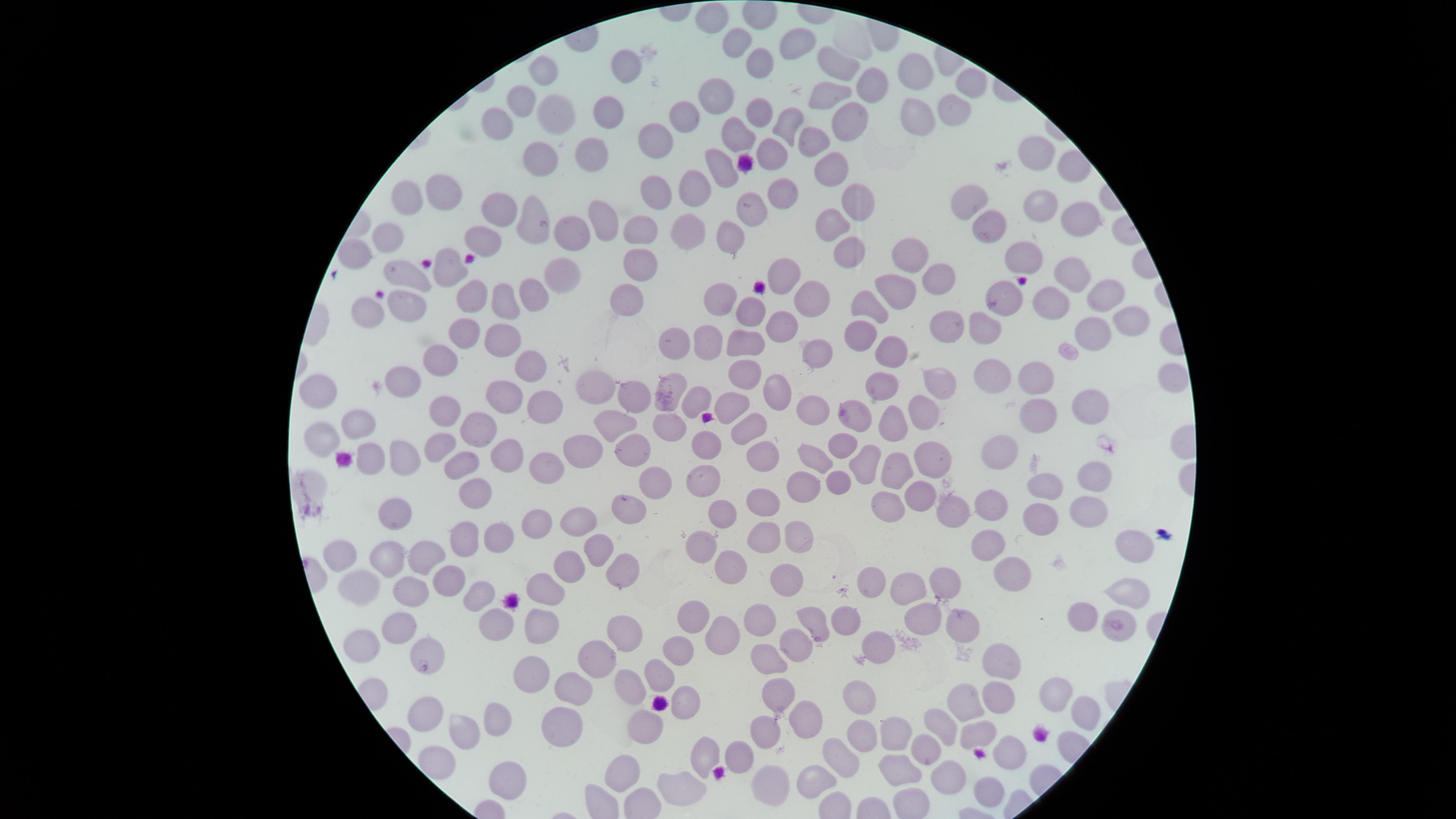
Approximate marker points as [x, y] in pixels. Uninfected RBCs: [712, 15], [790, 44], [732, 46], [762, 64], [625, 66], [838, 68], [917, 68], [547, 75], [873, 80], [969, 80], [718, 93], [835, 99], [525, 102], [950, 111], [561, 112], [612, 112], [760, 113], [680, 116], [916, 119], [850, 122], [502, 123], [781, 125], [736, 137], [818, 139], [654, 140], [540, 151], [1036, 151], [775, 153], [588, 159], [829, 170], [724, 175], [696, 189], [782, 193], [444, 194], [407, 198], [854, 201], [971, 201], [657, 202], [1039, 206], [500, 208], [755, 208], [532, 220], [604, 220], [1074, 220], [691, 229], [985, 231], [832, 232], [737, 234], [569, 236], [389, 237], [485, 239], [636, 239], [848, 249], [916, 253], [1024, 254], [360, 255], [447, 267], [644, 267], [1069, 271], [407, 273], [788, 273], [937, 274], [560, 279], [899, 285], [1006, 288], [1095, 290], [465, 297], [530, 298], [630, 298], [721, 298], [809, 299], [1050, 299], [496, 304], [871, 304], [405, 306], [750, 313], [371, 314], [783, 323], [1130, 323], [955, 324], [988, 325], [865, 329], [459, 334], [496, 338], [711, 338], [748, 338], [1094, 338], [674, 343], [891, 345], [813, 353], [442, 364], [528, 365], [1028, 370], [747, 371], [993, 374], [939, 378], [408, 382], [877, 385], [594, 392], [779, 392], [505, 394], [637, 394], [319, 395], [694, 397], [731, 400], [1088, 403], [553, 406], [444, 411], [811, 412], [924, 413], [1036, 414], [896, 419], [665, 421], [856, 421], [614, 426], [363, 430], [481, 431], [751, 431], [322, 440], [701, 440], [841, 441], [440, 446], [1006, 446], [581, 447], [765, 452], [631, 454], [369, 456], [402, 457], [509, 457], [928, 457], [815, 458], [453, 460], [898, 464], [862, 465], [544, 470], [1091, 470], [705, 475], [837, 478], [660, 485], [1043, 485], [473, 486], [799, 487], [918, 487], [765, 497], [990, 499], [886, 502], [1096, 507], [622, 508], [960, 508], [394, 512], [725, 515], [1041, 516], [576, 522], [536, 527], [794, 527], [758, 535], [497, 536], [460, 538], [703, 541], [978, 543], [598, 545], [1135, 547], [341, 552], [428, 553], [387, 555], [731, 563], [565, 564], [621, 565], [1004, 571], [873, 577], [946, 578], [453, 580], [411, 582], [911, 583], [350, 584], [784, 585], [545, 590], [1127, 590], [476, 591], [843, 612], [1084, 614], [918, 615], [695, 617], [491, 621], [540, 621], [758, 621], [810, 621], [966, 621], [394, 624], [1110, 626], [725, 628], [629, 632], [364, 640], [877, 641], [795, 644], [677, 647], [427, 653], [596, 654], [767, 656], [997, 660], [533, 673], [655, 674], [634, 681], [577, 689], [1055, 689], [863, 694], [997, 694], [779, 696], [965, 701], [679, 702], [422, 708], [1084, 712], [496, 715], [805, 717], [943, 722], [557, 726], [644, 726], [461, 731], [768, 733], [861, 733], [894, 734], [976, 735], [707, 748], [924, 750], [843, 754], [740, 755], [1017, 755], [622, 766], [898, 766], [817, 770], [948, 773], [504, 777], [771, 779], [679, 781], [991, 788]. Image is 1456×819 pixels. Thin blood film. Photographed with a smartphone camera through the microscope eyepiece. Giemsa stain. The visible region is circular. Single field of view. Presence: no malaria parasites detected.